Locate every blood parasite and identify its species.
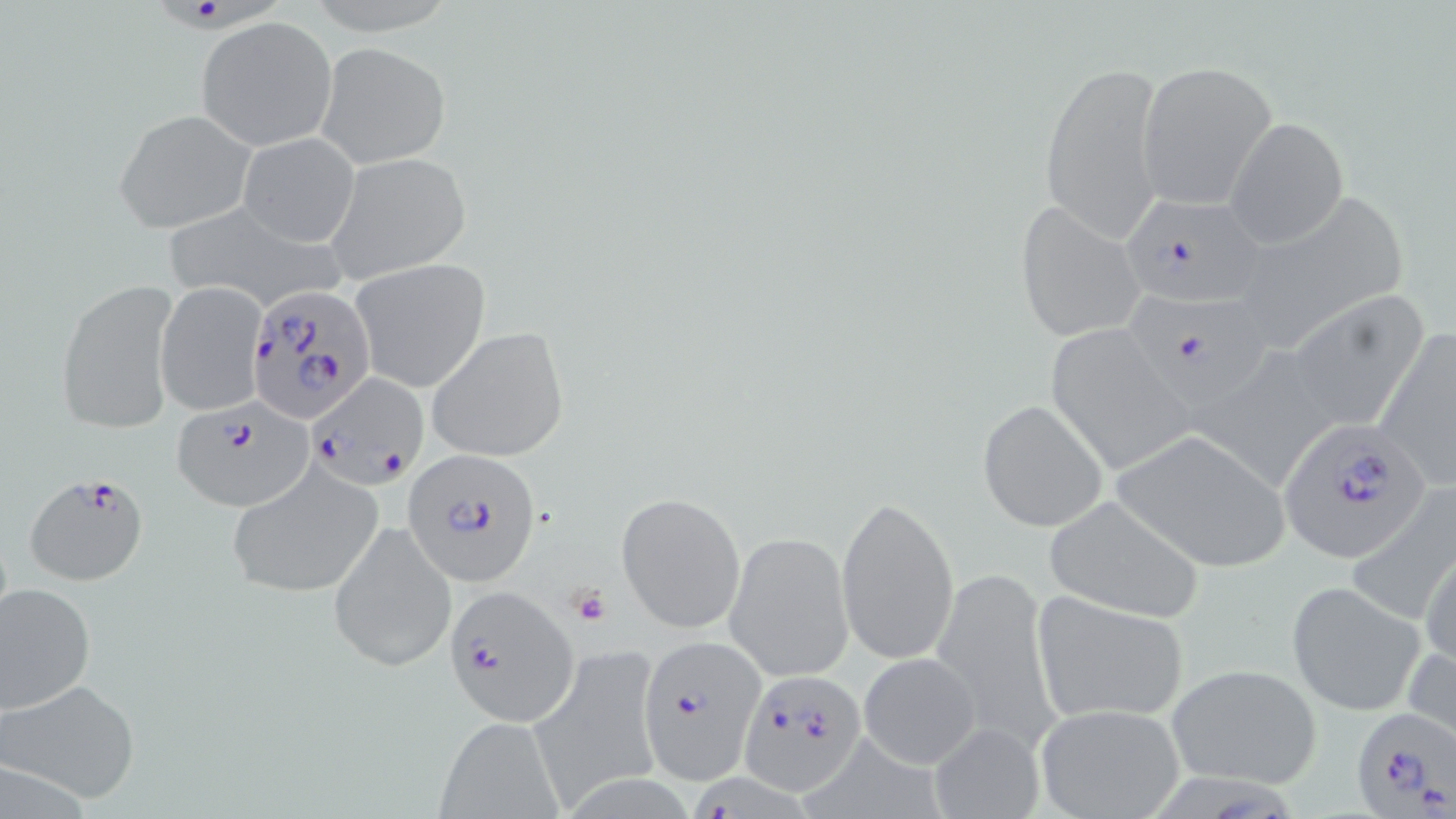

Approximate bounding boxes as [x1, y1, x2, y2] in pixels.
Plasmodium falciparum-infected red blood cells: [162, 2, 286, 36], [1117, 193, 1266, 306], [244, 281, 374, 424], [1129, 289, 1270, 408], [307, 373, 429, 490], [169, 400, 316, 511], [1276, 417, 1434, 566], [401, 450, 543, 589], [24, 471, 151, 587], [443, 583, 578, 727], [637, 634, 763, 783], [737, 669, 868, 795], [1349, 706, 1455, 816], [696, 774, 811, 819].
No Plasmodium ovale, Plasmodium malariae, Plasmodium vivax, Babesia divergens, or Trypanosoma brucei observed.

Summary:
  - Uninfected red blood cell locations: [195, 17, 337, 151], [316, 42, 450, 168], [1037, 59, 1167, 244], [1136, 61, 1277, 209], [114, 108, 256, 234], [1223, 116, 1348, 249], [238, 132, 359, 246], [322, 153, 472, 285], [1224, 190, 1412, 352], [157, 199, 344, 311], [1014, 201, 1147, 344], [350, 259, 491, 394], [53, 276, 182, 435], [155, 282, 268, 416], [1279, 289, 1431, 436], [1042, 321, 1193, 477], [1374, 323, 1456, 489], [427, 327, 569, 462], [977, 400, 1108, 532], [1111, 429, 1290, 572], [225, 463, 386, 600], [1348, 485, 1456, 623], [616, 491, 745, 634], [839, 494, 960, 669], [1041, 494, 1206, 624], [328, 519, 456, 673], [725, 530, 854, 683], [1420, 540, 1456, 674], [930, 564, 1059, 749], [0, 580, 96, 716], [1286, 581, 1426, 717], [1030, 590, 1190, 724], [1404, 637, 1456, 750], [528, 646, 664, 807], [857, 651, 983, 770], [1166, 663, 1322, 789], [2, 679, 140, 805], [1033, 703, 1186, 819], [437, 717, 562, 813], [928, 722, 1044, 816]
  - Platelet locations: [569, 585, 610, 627]
  - Slide-level diagnosis: Plasmodium falciparum
  - Preparation: thin blood smear
  - Magnification: 1000x
  - Modality: optical microscopy
  - Stain: May-Grünwald-Giemsa
  - Field of view: one of a larger specimen
  - Image size: 1456×819 pixels